Assess this cell for malaria.
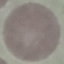

Uninfected.

capture = smartphone camera at the microscope eyepiece
image type = automatically extracted cell patch, resized to 64 × 64 pixels
preparation = thin blood film
stain = Giemsa